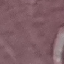 Malaria status: uninfected. Thin blood smear. Cell patch, automatically extracted from a larger field of view and resized to 64 × 64 pixels. Acquired by smartphone through the microscope eyepiece. Giemsa stain.